Classify this cell by malaria status.
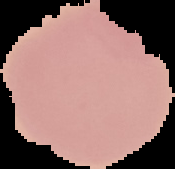

Uninfected.

Summary:
  - Image type: segmented cell region with the area outside set to black
  - Preparation: thin blood film
  - Image size: 175×169 pixels